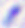 Micrograph. Toxoplasma gondii is seen. 400x magnification.